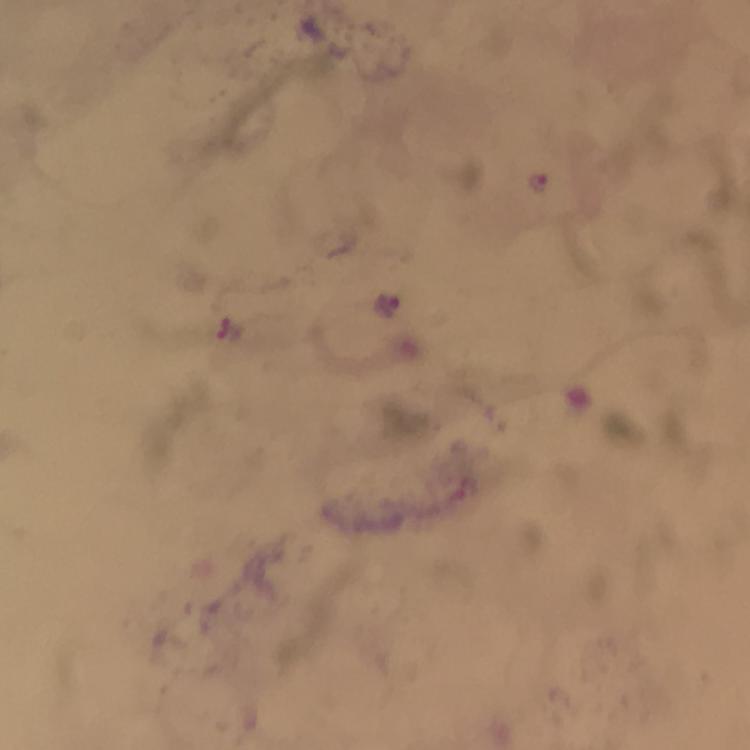
{
  "immersion_oil": "applied",
  "magnification": "100x",
  "context": "from a malaria diagnostic workup",
  "capture": "smartphone mounted on the microscope",
  "preparation": "thick blood film",
  "malaria_parasite_locations": "approximate object centers, in pixels from the top-left corner: (x=537, y=182), (x=388, y=303)",
  "stain": "Giemsa",
  "cropped_from": "a single field of view",
  "image_size": "750×750 pixels"
}